Report the malaria status of this cell.
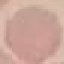
It is uninfected.

capture = smartphone through the microscope eyepiece
preparation = thin smear
stain = Giemsa
image type = cell patch, automatically extracted from a larger field of view and resized to 64 × 64 pixels